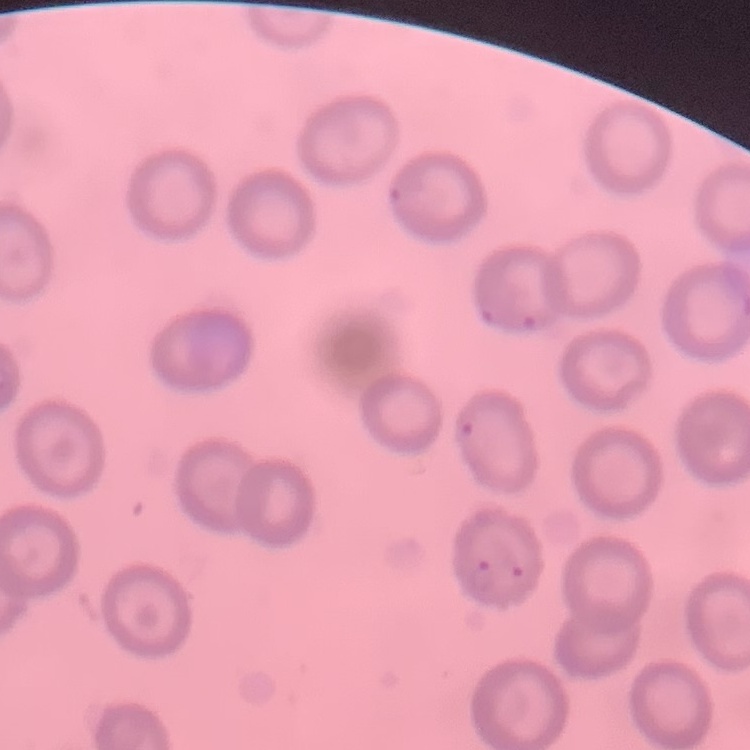 The red blood cells show no rouleaux formation. Field's or Giemsa stain. One tile cut from a larger photomicrograph. Thin peripheral smear.